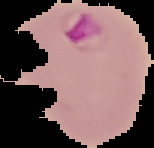

Malaria status: parasitized. The area outside the segmented cell region is set to black. Image is 154×148 pixels. From a thin blood smear.